Name the blood parasite species.
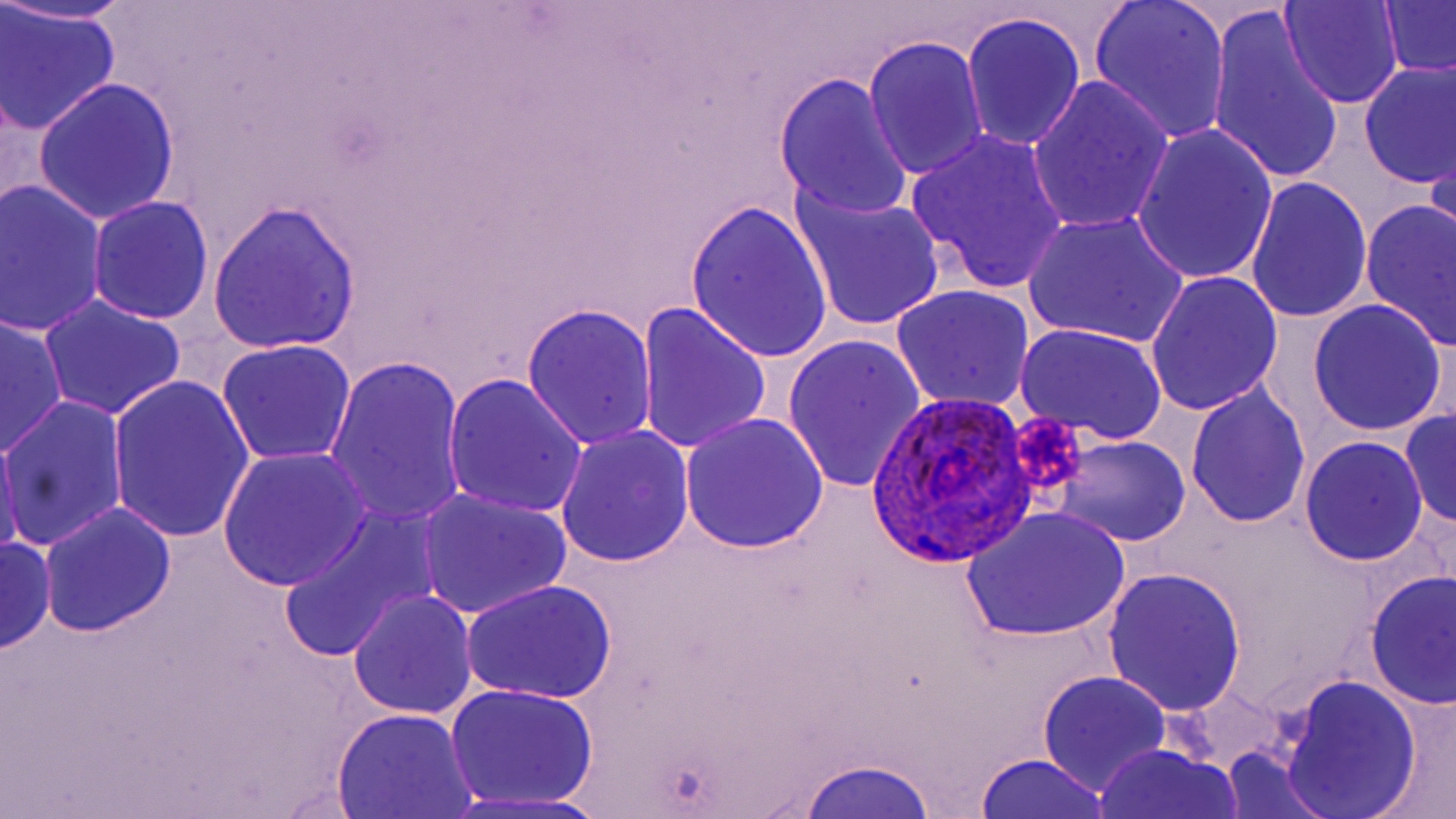
Plasmodium ovale.

Approximate bounding boxes as (x1, y1, x2, y2) in pixels. Platelet locations: (1004, 409, 1090, 499). Plasmodium ovale-infected red blood cell locations: (866, 392, 1032, 569). Uninfected red blood cell locations: (1, 0, 141, 25), (1087, 0, 1233, 144), (1279, 0, 1404, 109), (1377, 1, 1456, 82), (1, 6, 121, 135), (1208, 9, 1346, 188), (961, 13, 1086, 153), (863, 36, 991, 181), (1357, 59, 1455, 189), (773, 73, 914, 221), (1026, 77, 1175, 235), (31, 78, 181, 225), (1132, 125, 1280, 286), (905, 129, 1070, 295), (1427, 131, 1456, 268), (1247, 176, 1373, 325), (1, 181, 109, 336), (788, 183, 949, 336), (86, 196, 214, 326), (686, 198, 834, 366), (1359, 198, 1456, 352), (208, 200, 363, 354), (1023, 213, 1190, 348), (1145, 271, 1284, 415), (890, 285, 1035, 412), (39, 294, 187, 421), (1306, 298, 1448, 438), (637, 303, 772, 457), (522, 304, 657, 450), (0, 314, 67, 458), (1015, 322, 1168, 444), (782, 332, 927, 495), (216, 340, 356, 466), (325, 356, 468, 530), (108, 374, 257, 545), (443, 374, 589, 519), (1185, 382, 1310, 528), (1, 394, 128, 554), (1399, 408, 1456, 534), (678, 414, 829, 556), (0, 424, 22, 564), (556, 425, 694, 566), (1050, 437, 1191, 547), (1300, 437, 1428, 565), (219, 450, 370, 589), (416, 488, 572, 620), (39, 501, 177, 637), (961, 507, 1132, 643), (280, 508, 436, 663), (1, 532, 54, 656), (1102, 565, 1247, 716), (1365, 570, 1455, 710), (461, 578, 618, 705), (348, 591, 479, 720), (1037, 672, 1172, 796), (1276, 673, 1423, 819), (445, 683, 601, 809), (1369, 693, 1456, 819), (331, 709, 482, 819), (1093, 744, 1244, 819), (1219, 750, 1332, 819), (973, 751, 1117, 818), (795, 755, 939, 818), (447, 790, 615, 819). Image is 1456×819 pixels. Thin blood film. 1000x magnification. May-Grünwald-Giemsa-stained preparation. Single field of view. Optical microscopy.